Outline each blood parasite and name the species.
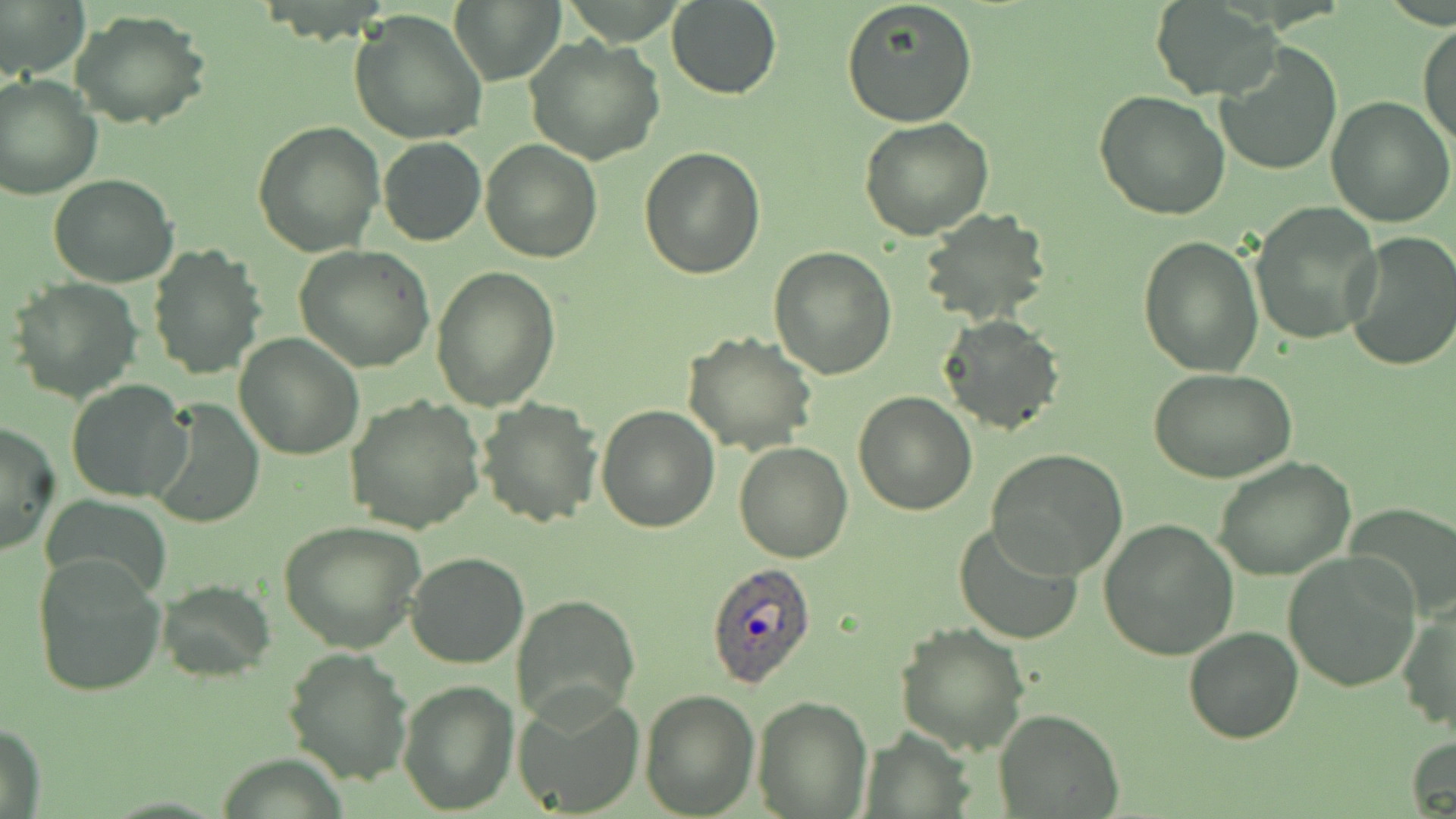
Approximate bounding boxes as [x1, y1, x2, y2] in pixels.
Plasmodium ovale-infected red blood cells: [705, 562, 817, 689].
No Plasmodium falciparum, Plasmodium malariae, Plasmodium vivax, Babesia divergens, or Trypanosoma brucei observed.

slide-level diagnosis = Plasmodium ovale
preparation = thin blood smear
uninfected red blood cell locations = approximate bounding boxes as [x1, y1, x2, y2] in pixels: [0, 0, 89, 77], [666, 0, 781, 100], [839, 0, 979, 127], [449, 1, 564, 85], [1152, 3, 1280, 100], [70, 9, 211, 128], [349, 9, 488, 146], [1418, 23, 1456, 150], [524, 36, 665, 165], [1214, 43, 1343, 177], [0, 74, 101, 200], [1094, 90, 1230, 223], [1326, 96, 1456, 227], [251, 118, 385, 257], [860, 119, 994, 241], [378, 137, 486, 246], [480, 140, 601, 262], [639, 148, 766, 280], [48, 173, 180, 288], [1249, 202, 1382, 344], [916, 209, 1054, 329], [1343, 232, 1456, 371], [1136, 235, 1264, 377], [147, 246, 265, 379], [294, 246, 435, 373], [767, 246, 896, 378], [431, 266, 561, 411], [8, 277, 144, 404], [939, 313, 1064, 436], [681, 331, 819, 457], [234, 333, 365, 460], [1147, 366, 1298, 484], [66, 379, 191, 503], [852, 391, 978, 515], [149, 396, 264, 528], [345, 396, 486, 534], [475, 397, 603, 527], [596, 404, 721, 533], [0, 420, 60, 558], [734, 442, 853, 562], [986, 449, 1128, 580], [1212, 456, 1356, 581], [42, 491, 172, 600], [1346, 507, 1455, 624], [1098, 518, 1239, 662], [278, 519, 427, 653], [953, 521, 1084, 646], [405, 552, 529, 669], [1283, 552, 1422, 691], [31, 553, 167, 699], [154, 580, 275, 680], [512, 594, 640, 724], [1396, 602, 1455, 738], [895, 623, 1028, 755], [1184, 628, 1302, 743], [282, 647, 414, 786], [398, 679, 521, 815], [639, 687, 759, 816], [512, 690, 644, 818], [752, 695, 872, 817], [995, 709, 1123, 817], [1, 722, 47, 819], [1406, 736, 1456, 819]
image size = 1456×819 pixels
field of view = one of a larger specimen
stain = May-Grünwald-Giemsa
modality = optical microscopy
magnification = 1000x